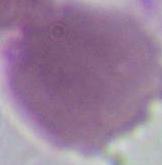
An erythrocyte is seen. 1000x magnification. Photomicrograph.